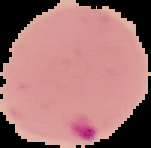
image size = 151×148 pixels
image type = segmented cell region on a black background
preparation = thin blood smear
result = malaria parasites detected